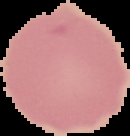
Summary:
  - Preparation: thin blood smear
  - Malaria status: uninfected
  - Image type: cell region segmented out of the field of view; surrounding area masked to black
  - Image size: 130×136 pixels